Report the malaria status of this cell.
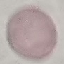
Uninfected.

stain = Giemsa
image type = cell patch, automatically extracted from a larger field of view and resized to 64 × 64 pixels
capture = smartphone camera at the microscope eyepiece
preparation = thin blood smear